Name the parasite shown.
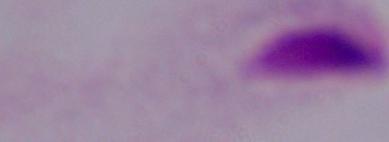

A trichomonad.

modality = photomicrograph
magnification = 1000x